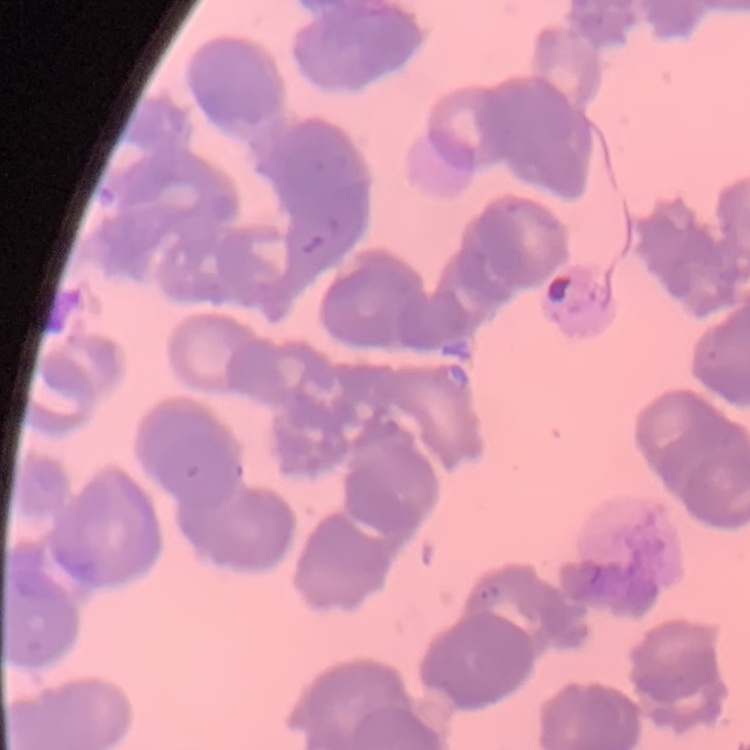

The red blood cells show rouleaux formation. Stained with either Field's or Giemsa. One tile cut from a larger photomicrograph. Thin blood smear.